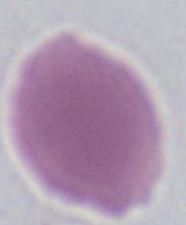

Summary:
  - Modality: photomicrograph
  - Magnification: 1000x
  - Identification: red blood cell